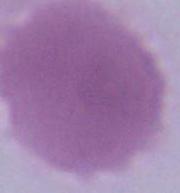

Summary:
  - Magnification: 1000x
  - Modality: micrograph
  - Identification: erythrocyte